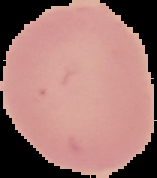
Malaria status: uninfected. From a thin blood film. Image is 157×178 pixels. Cell region segmented out of the field of view; the surrounding area is masked to black.